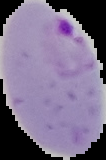

Summary:
  - Preparation: thin blood smear
  - Image size: 106×160 pixels
  - Image type: segmented cell region on a black background
  - Result: malaria parasites detected